Identify the parasite.
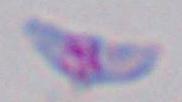

This is Toxoplasma gondii.

Summary:
  - Magnification: 1000x
  - Modality: photomicrograph